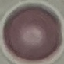
Result: negative for malaria parasites. Cell patch, automatically extracted from a larger field of view and resized to 64 × 64 pixels. Giemsa-stained preparation. Thin blood smear. Acquired by smartphone through the microscope eyepiece.